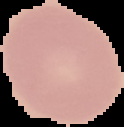

Summary:
  - Result: negative for Plasmodium parasites
  - Image size: 124×127 pixels
  - Image type: segmented cell region with the area outside set to black
  - Preparation: thin blood smear